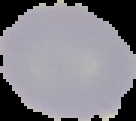

Summary:
  - Preparation: thin blood film
  - Image size: 136×121 pixels
  - Result: no Plasmodium parasites detected
  - Image type: segmented cell region on a black background